Locate every Plasmodium parasite.
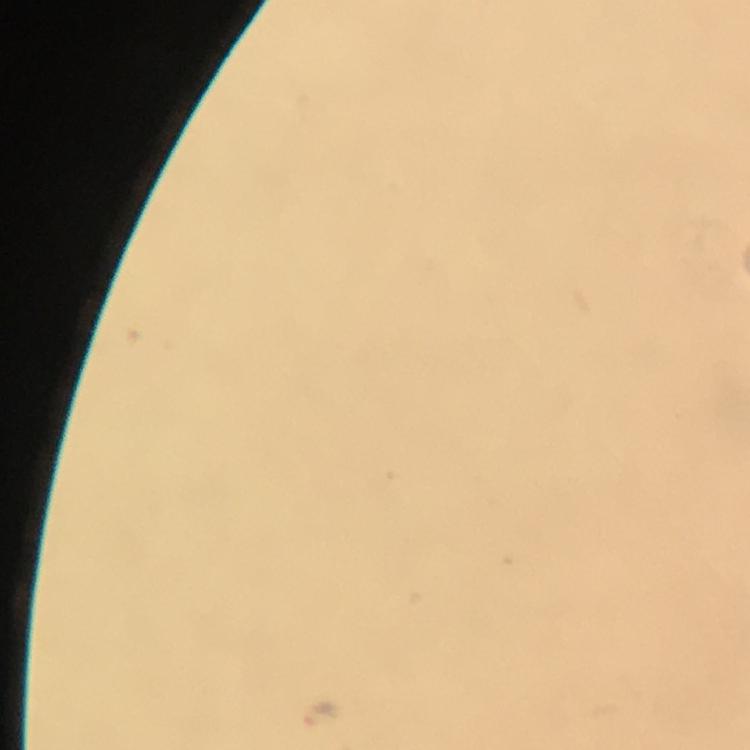
Approximate centers as [x, y] in pixels.
Plasmodium parasites: [320, 713].

Giemsa stain. Cropped region of a single field of view. From a malaria diagnostic workup. Photographed with a smartphone mounted on the microscope. Thick smear. At 100x magnification. Immersion oil was used. Image is 750×750 pixels.